Assess this cell for malaria.
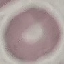
Uninfected.

Summary:
  - Capture: smartphone through the microscope eyepiece
  - Stain: Giemsa
  - Preparation: thin smear
  - Image type: automatically extracted cell patch, resized to 64 × 64 pixels